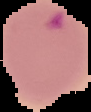

Summary:
  - Image type: segmented cell region with the area outside set to black
  - Preparation: thin blood film
  - Result: malaria parasites detected
  - Image size: 91×112 pixels